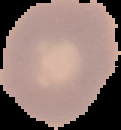 Image is 121×130 pixels. Malaria status: uninfected. From a thin blood smear. The area outside the segmented cell region is set to black.